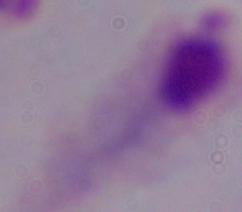
Photomicrograph. A trichomonad is shown. 1000x magnification.